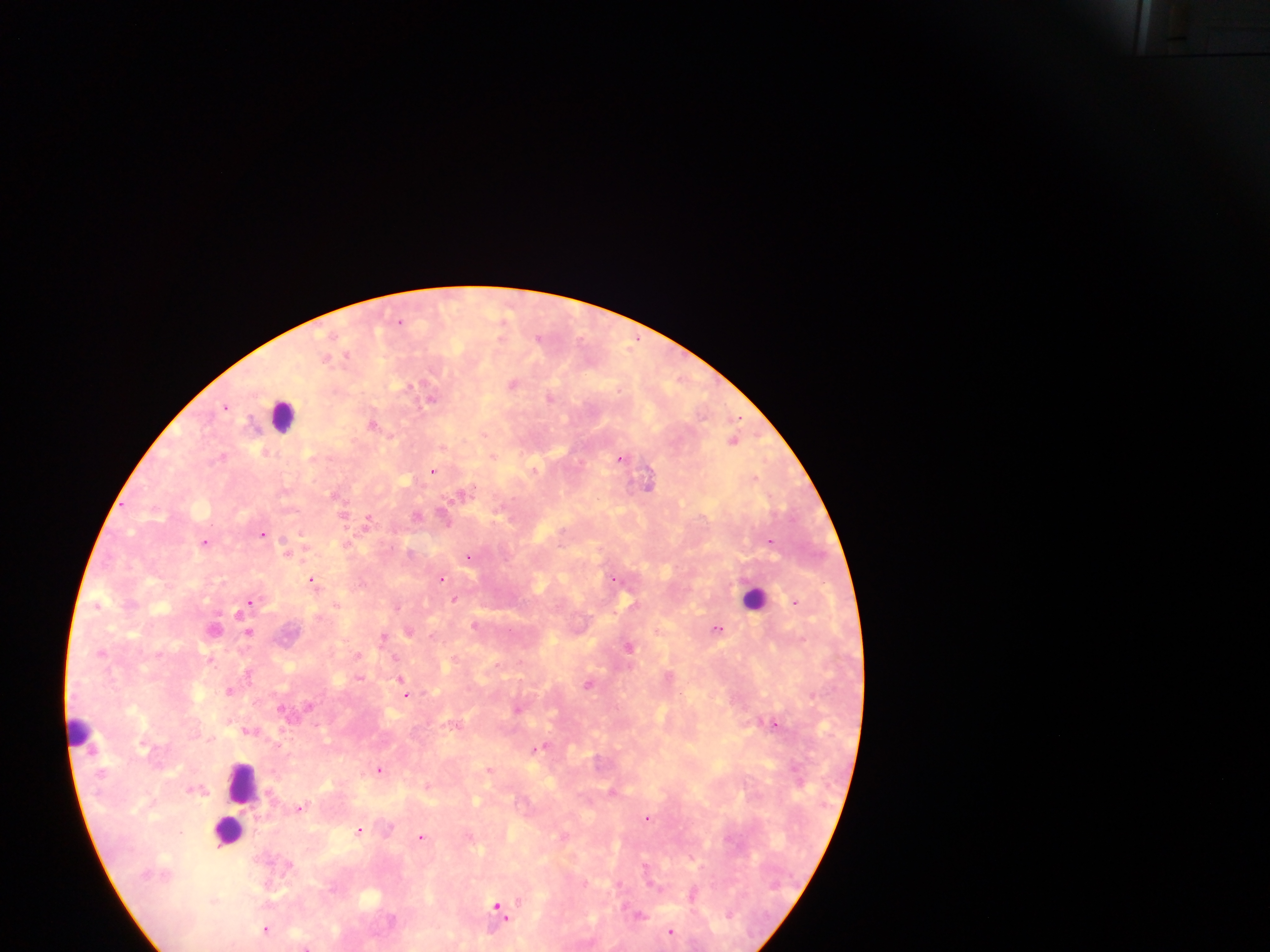
country = Ghana
Plasmodium parasite locations = approximate centers as [x, y] in pixels: [400, 321], [327, 356], [512, 384], [409, 385], [550, 396], [434, 399], [224, 407], [372, 423], [485, 432], [734, 439], [494, 455], [625, 457], [434, 470], [649, 483], [334, 494], [345, 515], [443, 515], [368, 521], [263, 533], [204, 542], [771, 544], [288, 552], [469, 558], [442, 577], [312, 580], [455, 599], [249, 600], [797, 602], [97, 605], [338, 605], [399, 608], [475, 625], [719, 628], [250, 632], [410, 632], [385, 637], [629, 646], [210, 658], [396, 659], [249, 674], [400, 675], [229, 690], [404, 690], [775, 722], [248, 729], [535, 749], [380, 769], [490, 769], [428, 786], [191, 789], [478, 800], [299, 807], [648, 818], [359, 829], [421, 835], [646, 860], [369, 898], [520, 898], [212, 899], [497, 905], [266, 929], [672, 930]
image size = 1270×952 pixels
field of view = single
preparation = thick blood film
capture = mobile-phone photograph through a microscope
leukocyte locations = approximate centers as [x, y] in pixels: [284, 419], [756, 594], [78, 730], [241, 784], [227, 831]